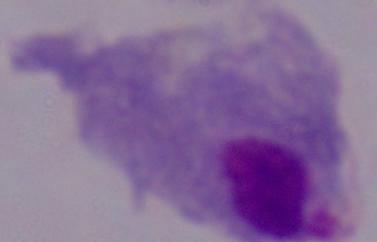

Captured at 1000x magnification. A trichomonad is seen. Micrograph.